Classify the preparation.
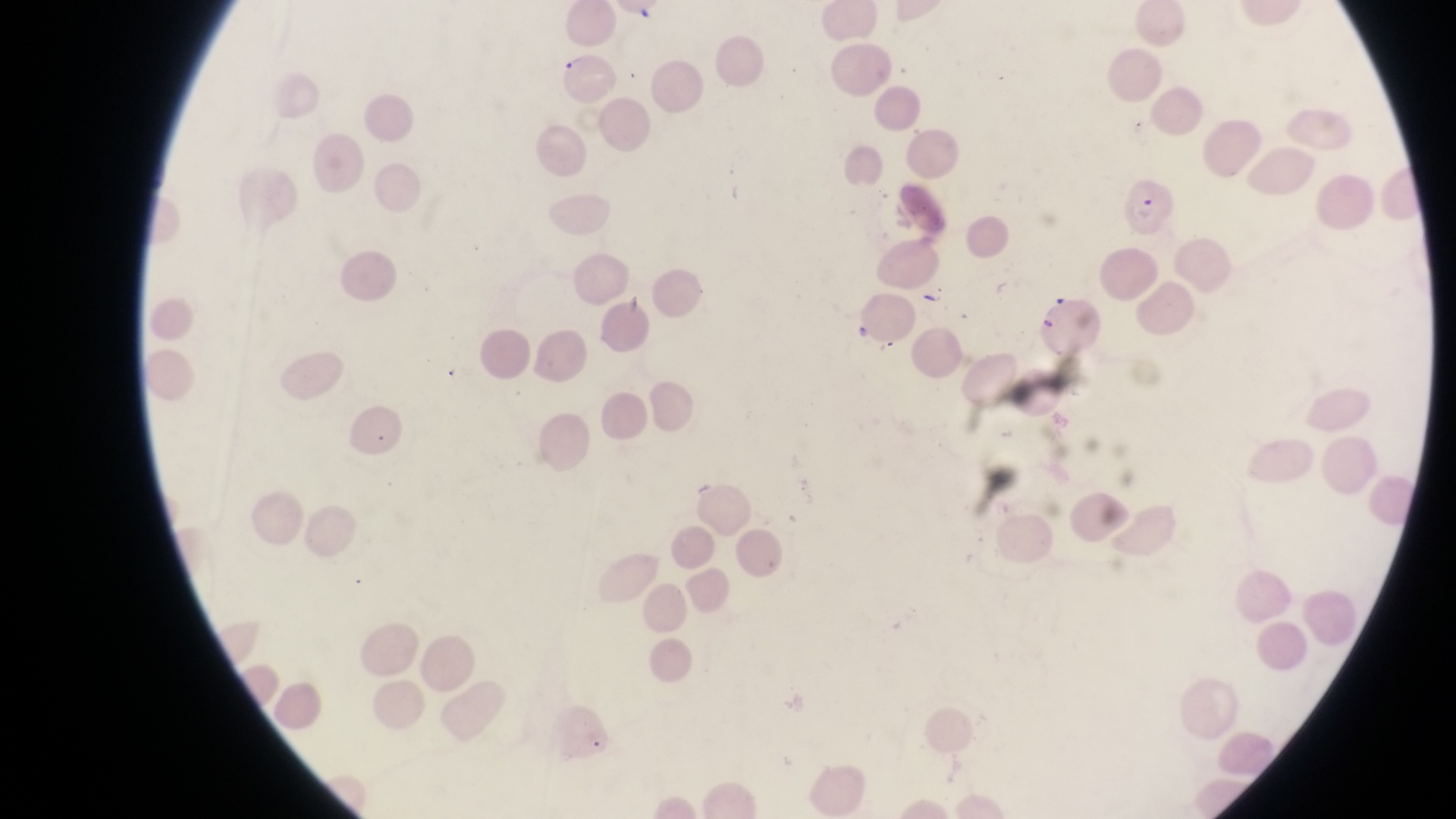
Thin blood film.

parasitised red blood cell locations = approximate bounding boxes as (left, top, right, bottom) in pixels: (558, 52, 617, 105), (1120, 174, 1180, 241), (1028, 280, 1102, 360)
capture = smartphone photograph through the eyepiece of an Olympus CX-23 microscope
image size = 1456×819 pixels
artifact (platelet-like body, stain precipitate, or debris) locations = approximate bounding boxes as (left, top, right, bottom) in pixels: (920, 278, 949, 305)
field of view = single
country = Uganda
magnification = 1000x